Assess this cell for malaria.
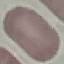
It is uninfected.

Summary:
  - Preparation: thin blood film
  - Image type: automatically extracted cell patch, resized to 64 × 64 pixels
  - Stain: Giemsa
  - Capture: smartphone camera at the microscope eyepiece